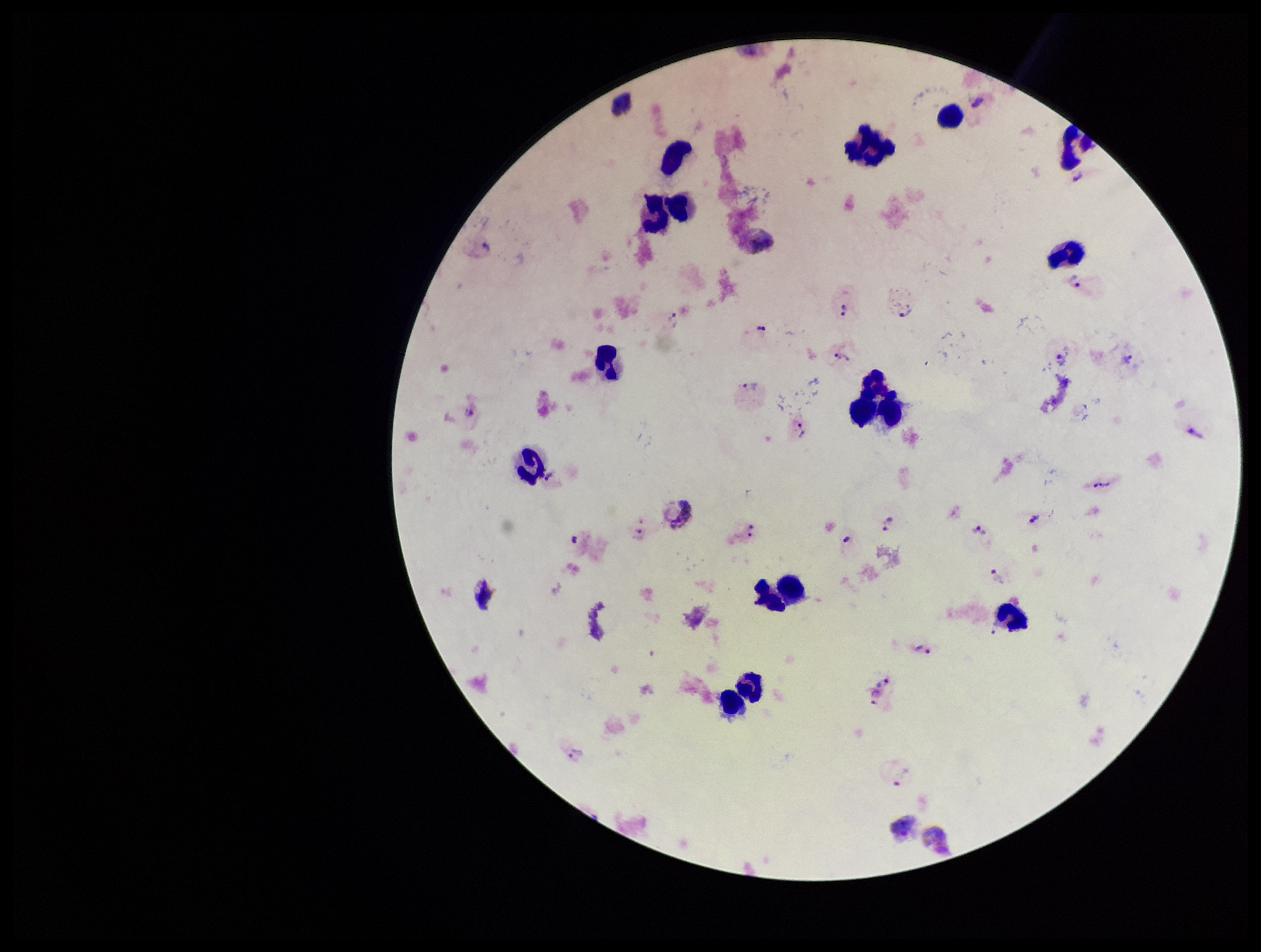
image size = 1261×952 pixels
parasite count = 34
capture = smartphone photograph through the microscope eyepiece
Plasmodium parasites = identified
preparation = thick smear
stain = Giemsa
field of view = one from this slide
patient malaria status = infected
leukocyte count = 17
species reported for this patient = Plasmodium vivax